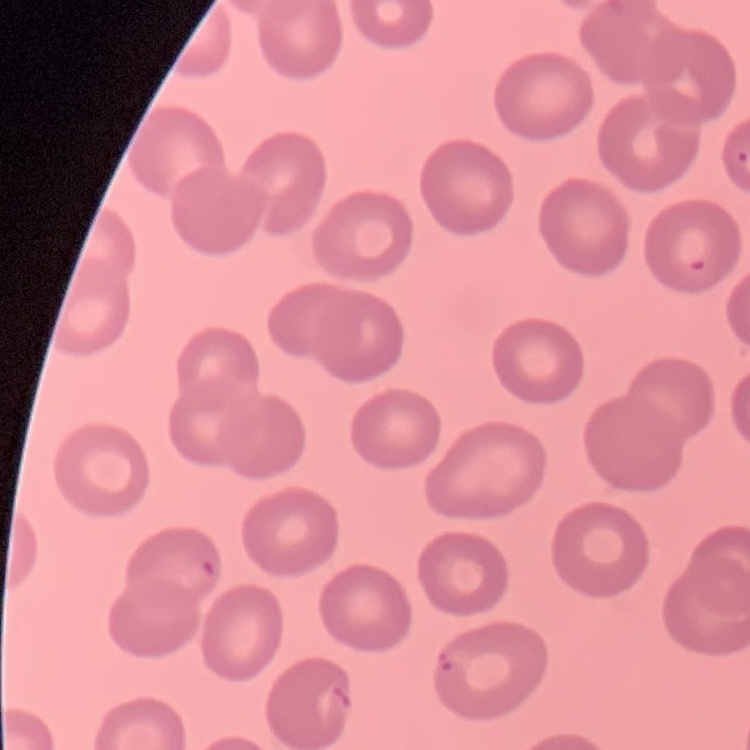

red blood cell morphology = no rouleaux formation
stain = Field's or Giemsa
preparation = thin peripheral smear
image type = square crop of a larger photomicrograph